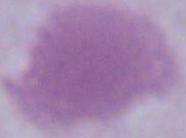 A red blood cell is seen. 1000x magnification. Photomicrograph.